Which red blood cells are Plasmodium falciparum-infected, and which are of indeterminate infection status?
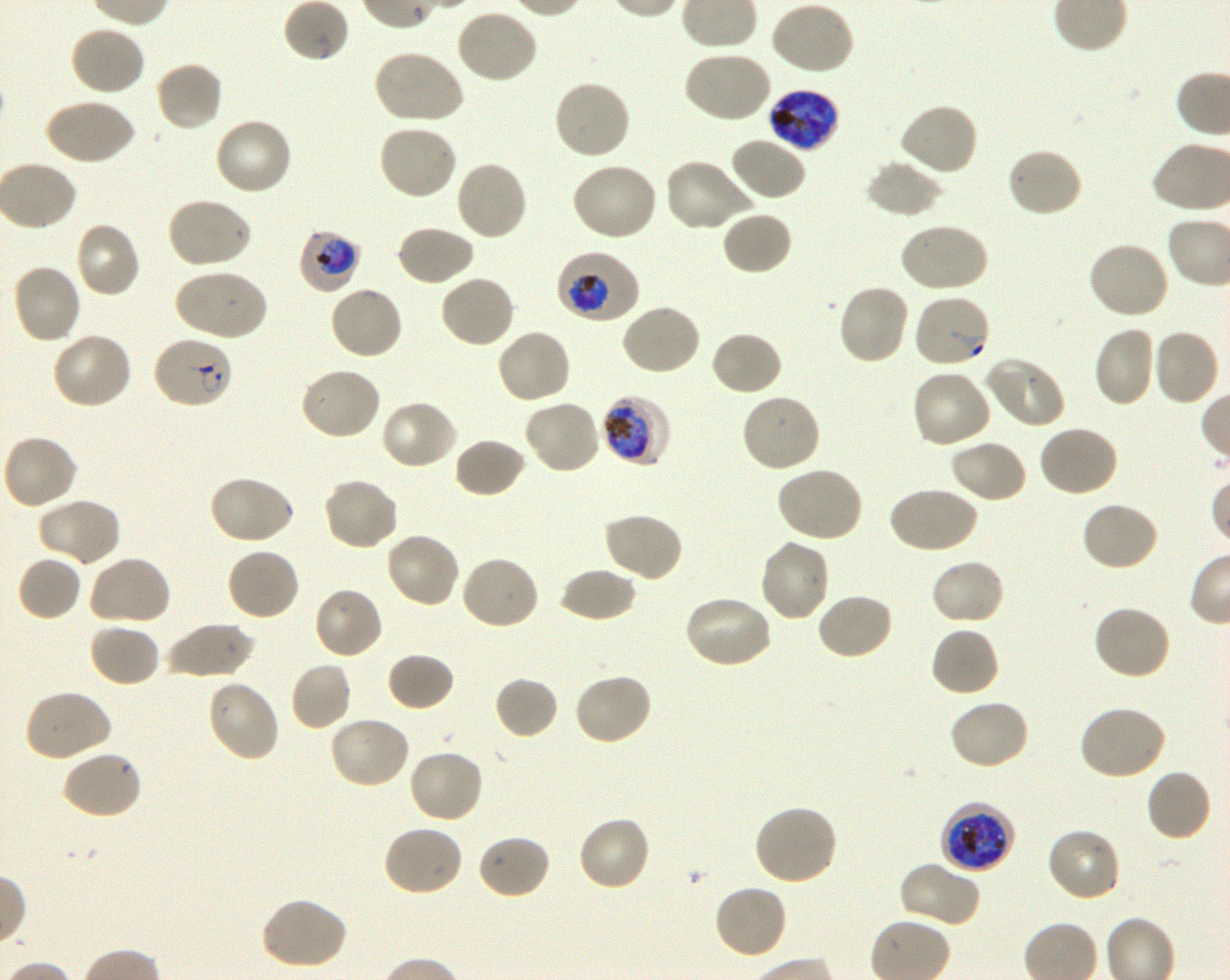
Approximate bounding boxes as [x1, y1, x2, y2] in pixels. Not every red blood cell is marked. A life-cycle stage — or a range of stages, where the recorded stages span more than one — follows each staged infected red blood cell.
Infected red blood cells: [767, 89, 841, 152] late trophozoite to late schizont; [299, 229, 360, 294] trophozoite; [556, 251, 640, 325] trophozoite; [151, 336, 235, 410] ring; [601, 393, 671, 467] early trophozoite to late schizont; [939, 801, 1016, 874] late trophozoite to late schizont.
Red blood cells of indeterminate infection status: [913, 293, 991, 369].

Summary:
  - Locations of uninfected red blood cells: [283, 0, 350, 63], [769, 1, 855, 76], [455, 8, 538, 84], [69, 25, 146, 98], [372, 49, 465, 125], [682, 51, 772, 124], [155, 60, 224, 132], [553, 80, 632, 161], [44, 97, 135, 166], [898, 102, 979, 177], [213, 117, 294, 197], [377, 123, 458, 200], [729, 135, 808, 202], [1005, 146, 1083, 218], [664, 158, 754, 233], [864, 159, 943, 219], [455, 160, 529, 241], [571, 161, 659, 241], [165, 196, 253, 270], [721, 210, 793, 276], [74, 220, 142, 298], [897, 222, 988, 293], [396, 224, 475, 286], [1088, 240, 1171, 319], [11, 263, 82, 345], [173, 268, 268, 342], [439, 274, 515, 349], [837, 283, 911, 366], [329, 284, 404, 361], [620, 303, 703, 376], [1092, 326, 1156, 408], [496, 328, 573, 405], [1151, 328, 1221, 407], [710, 330, 784, 397], [51, 332, 135, 410], [983, 356, 1065, 430], [299, 367, 382, 441], [911, 368, 994, 449], [740, 393, 821, 474], [524, 397, 603, 475], [379, 399, 458, 470], [1037, 425, 1119, 498], [1, 434, 79, 511], [453, 437, 527, 498], [949, 439, 1028, 504], [776, 465, 864, 543], [207, 475, 295, 545], [321, 477, 399, 552], [887, 486, 978, 554], [36, 496, 122, 567], [1080, 500, 1160, 571], [601, 511, 684, 583], [384, 532, 462, 610], [758, 538, 831, 623], [226, 546, 300, 622], [459, 553, 540, 630], [88, 554, 172, 627], [17, 555, 82, 622], [930, 558, 1005, 626], [559, 567, 637, 622], [312, 586, 385, 660], [816, 592, 895, 661], [683, 594, 774, 669], [1093, 603, 1172, 681], [162, 622, 258, 678], [88, 623, 161, 688], [930, 625, 1000, 697], [386, 651, 455, 713], [290, 661, 352, 731], [572, 672, 653, 747], [493, 676, 559, 740], [205, 679, 281, 764], [22, 689, 113, 764], [948, 699, 1031, 771], [1077, 705, 1167, 781], [328, 714, 411, 789], [408, 748, 485, 824], [61, 749, 144, 820], [1145, 769, 1212, 843], [754, 805, 839, 887], [577, 815, 652, 892], [382, 824, 464, 897], [1046, 827, 1121, 903], [476, 833, 552, 900], [898, 861, 982, 929], [712, 883, 788, 961], [260, 896, 348, 971]
  - Life-cycle stages observed: ring, trophozoite
  - Preparation: thin blood smear
  - Donor blood group: O+
  - Objective: 100x, oil immersion, numerical aperture 1.30
  - Field of view: single
  - Image size: 1230×980 pixels
  - Culture: Plasmodium falciparum strain 3D7, shaking, in vitro
  - Stain: Giemsa